Identify the cell.
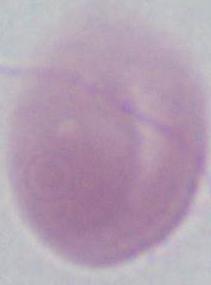
This is an erythrocyte.

modality: photomicrograph
magnification: 1000x